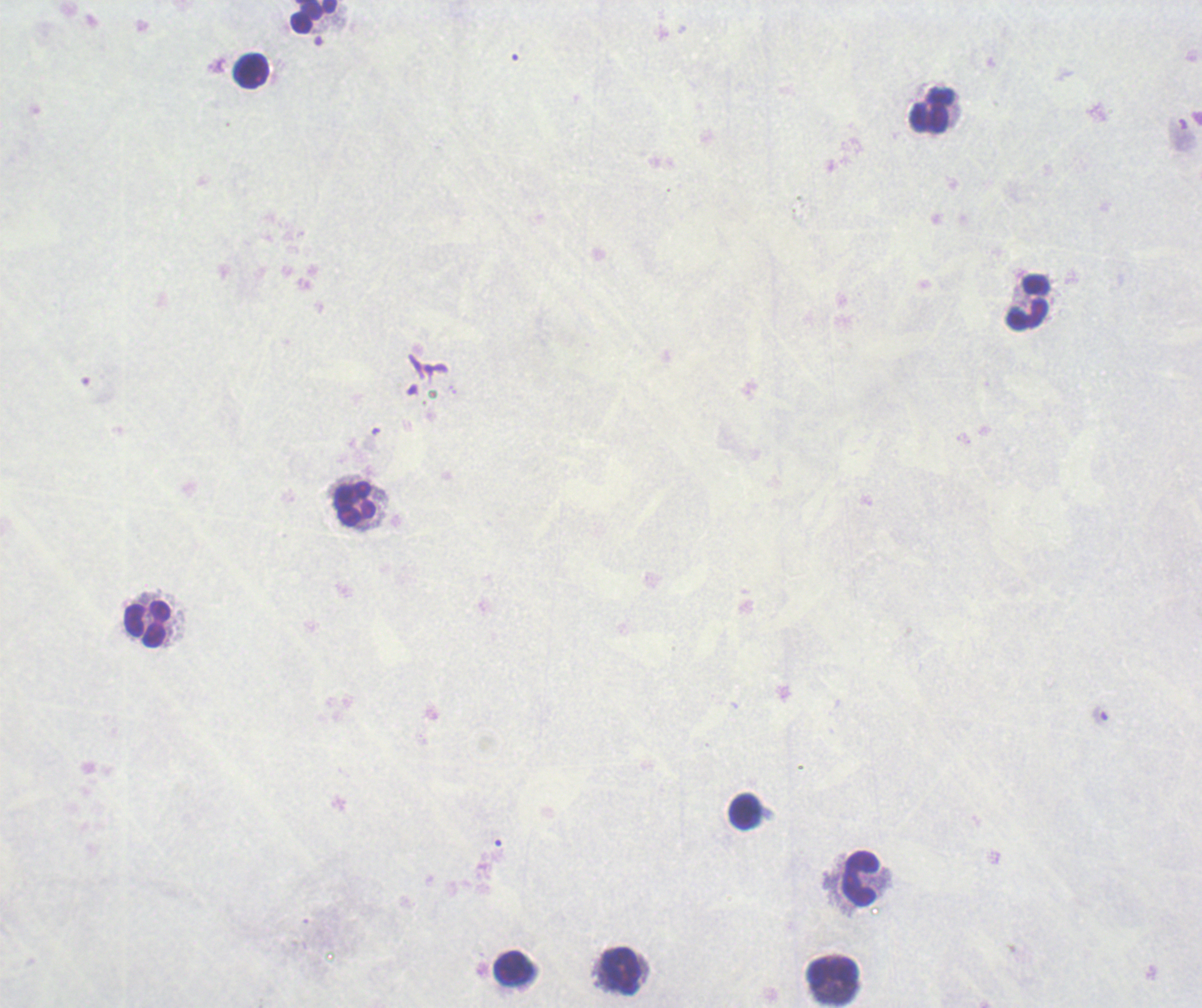

Approximate centers as (x, y) in pixels.
Summary:
  - Leukocyte locations: (313, 17), (252, 71), (932, 112), (1028, 302), (355, 504), (148, 624), (744, 811), (860, 878), (515, 969), (621, 972), (832, 973)
  - Background quality: poor
  - Image size: 1202×1008 pixels
  - Field of view: single
  - Magnification: 100x
  - Preparation: thick blood film
  - Result: no malaria parasites seen
  - Context: previously used in an actual diagnosis
  - Stain: Romanowsky